Give the extent of all Plasmodium falciparum-infected red blood cells.
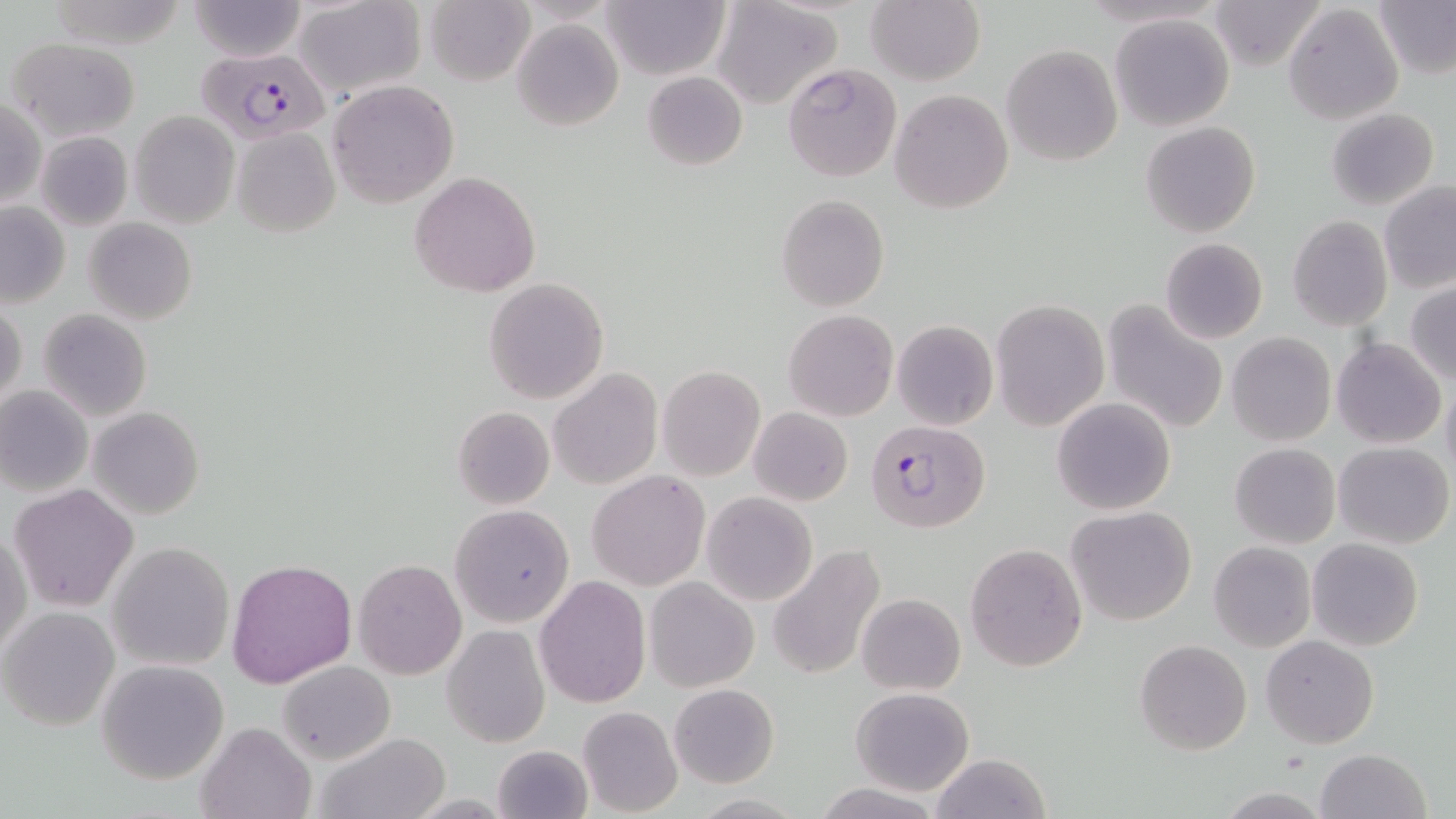
Approximate bounding boxes as (x1, y1, x2, y2) in pixels.
Plasmodium falciparum-infected red blood cells: (196, 47, 331, 144), (866, 418, 989, 534).

Summary:
  - Uninfected red blood cell locations: (44, 0, 191, 50), (1207, 0, 1324, 71), (189, 1, 306, 62), (293, 1, 426, 98), (602, 1, 727, 80), (712, 1, 841, 110), (866, 1, 985, 86), (1376, 1, 1456, 78), (425, 2, 533, 85), (1281, 4, 1404, 125), (1110, 12, 1234, 131), (512, 19, 623, 132), (9, 37, 142, 141), (1001, 45, 1122, 166), (780, 63, 902, 182), (642, 71, 747, 172), (326, 80, 461, 207), (890, 90, 1015, 213), (0, 98, 46, 206), (1325, 107, 1439, 210), (130, 111, 240, 228), (1141, 120, 1259, 238), (231, 128, 340, 236), (35, 130, 134, 230), (410, 172, 541, 297), (1379, 181, 1456, 292), (776, 195, 889, 312), (0, 201, 70, 306), (1287, 216, 1392, 330), (83, 218, 197, 325), (1161, 237, 1268, 343), (484, 278, 609, 404), (1406, 284, 1456, 384), (990, 299, 1109, 430), (1103, 299, 1230, 435), (0, 303, 26, 413), (37, 309, 154, 423), (783, 311, 897, 422), (892, 319, 998, 431), (1227, 333, 1336, 446), (1333, 338, 1446, 449), (657, 366, 766, 482), (550, 368, 662, 492), (1442, 378, 1456, 483), (0, 386, 93, 497), (1052, 396, 1176, 515), (87, 406, 205, 519), (451, 406, 554, 509), (749, 407, 853, 506), (1334, 441, 1453, 548), (1230, 443, 1341, 549), (588, 470, 709, 590), (9, 482, 139, 612), (702, 492, 818, 606), (450, 503, 575, 629), (1067, 506, 1197, 626), (1, 527, 30, 660), (1307, 538, 1424, 650), (1208, 541, 1316, 651), (108, 543, 233, 670), (965, 543, 1088, 671), (770, 546, 887, 682), (226, 558, 357, 689), (354, 559, 466, 679), (534, 577, 650, 706), (645, 577, 758, 692), (855, 593, 966, 696), (0, 607, 118, 731), (443, 624, 549, 748), (1261, 634, 1379, 747), (1135, 638, 1252, 755), (96, 659, 229, 784), (279, 660, 394, 764), (668, 684, 780, 788), (851, 686, 975, 795), (577, 705, 683, 817), (196, 720, 315, 819), (313, 731, 450, 819), (491, 743, 593, 819), (1317, 747, 1431, 819), (929, 752, 1054, 819), (811, 782, 946, 819), (1213, 787, 1335, 819), (689, 794, 812, 818)
  - Slide-level diagnosis: Plasmodium falciparum
  - Image size: 1456×819 pixels
  - Magnification: 1000x
  - Modality: light microscopy
  - Preparation: thin blood film
  - Field of view: single
  - Stain: May-Grünwald-Giemsa